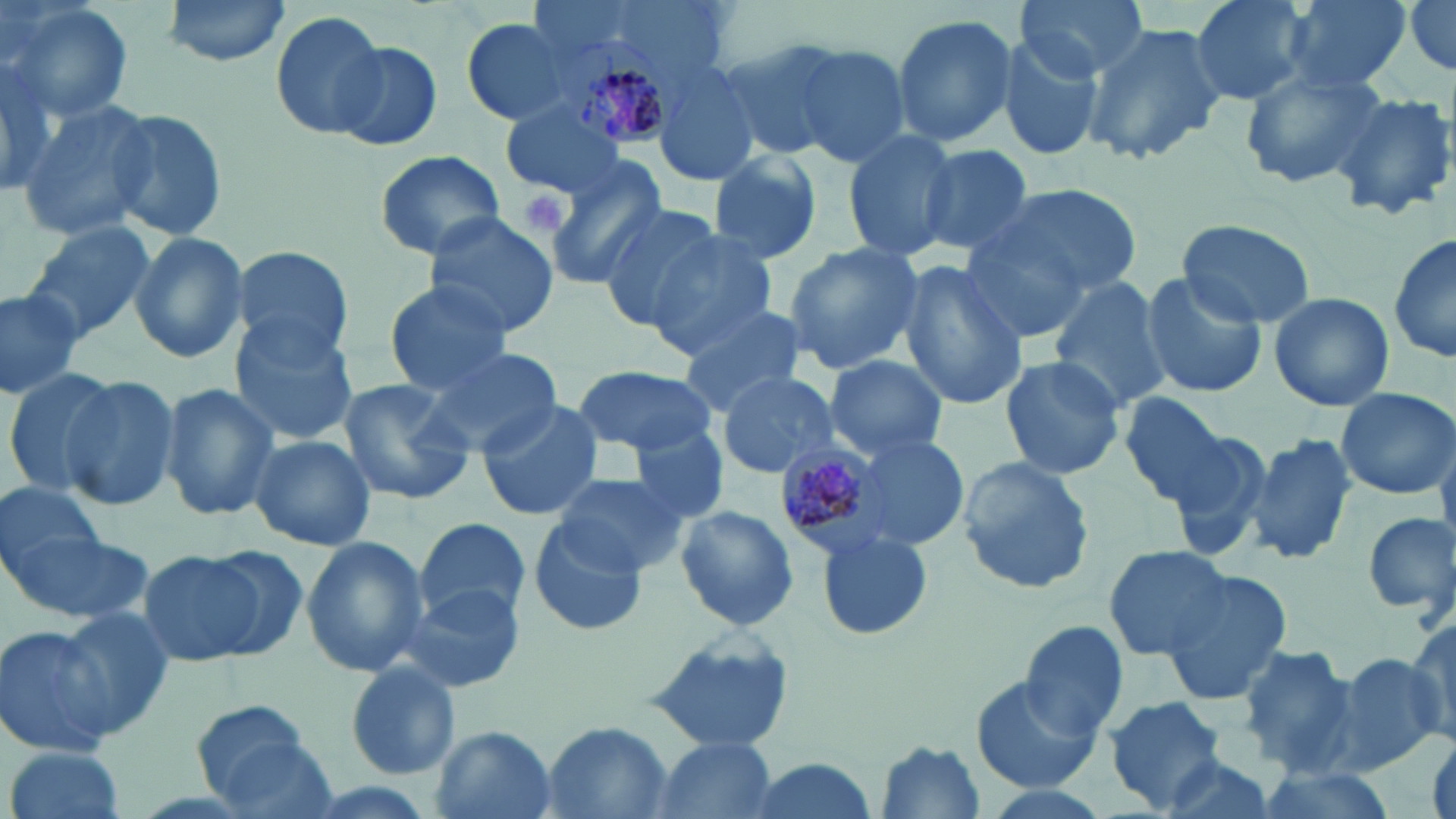

Approximate bounding boxes as [x1, y1, x2, y2] in pixels. Uninfected red blood cell locations: [3, 0, 135, 122], [159, 0, 295, 67], [1015, 0, 1145, 80], [1190, 0, 1312, 105], [1277, 0, 1415, 95], [1402, 0, 1456, 78], [270, 10, 391, 140], [461, 11, 593, 127], [891, 15, 1018, 146], [1083, 22, 1225, 168], [993, 29, 1104, 164], [717, 35, 851, 160], [327, 39, 442, 149], [788, 43, 913, 171], [0, 44, 62, 200], [653, 62, 762, 188], [1241, 62, 1388, 191], [1330, 92, 1454, 220], [18, 98, 156, 242], [499, 102, 628, 199], [107, 108, 230, 244], [841, 129, 958, 262], [915, 143, 1035, 258], [371, 149, 507, 259], [707, 150, 824, 266], [544, 158, 666, 287], [997, 181, 1145, 299], [597, 203, 726, 329], [421, 213, 560, 338], [956, 214, 1100, 340], [1175, 219, 1316, 328], [21, 220, 155, 340], [128, 233, 250, 363], [645, 234, 777, 356], [1390, 234, 1455, 365], [785, 243, 927, 371], [228, 246, 358, 366], [896, 259, 1029, 409], [1138, 273, 1266, 399], [1046, 278, 1171, 409], [383, 280, 515, 393], [0, 286, 87, 399], [1267, 290, 1395, 412], [675, 301, 808, 418], [229, 320, 361, 445], [419, 344, 564, 456], [823, 353, 948, 459], [996, 355, 1127, 481], [570, 366, 718, 457], [2, 368, 121, 498], [715, 371, 840, 479], [60, 377, 181, 510], [334, 379, 476, 505], [157, 382, 279, 521], [1336, 387, 1455, 498], [1115, 389, 1245, 513], [475, 398, 604, 521], [630, 431, 728, 526], [1244, 432, 1357, 570], [247, 434, 376, 551], [854, 435, 969, 548], [954, 457, 1095, 595], [551, 473, 687, 577], [0, 480, 114, 592], [674, 505, 800, 631], [1360, 511, 1455, 619], [532, 513, 649, 635], [414, 516, 532, 625], [7, 517, 154, 628], [814, 528, 933, 643], [301, 535, 430, 678], [1102, 544, 1236, 659], [136, 547, 283, 669], [1158, 568, 1298, 705], [400, 582, 526, 694], [52, 607, 179, 737], [1405, 618, 1456, 740], [1018, 621, 1129, 740], [0, 623, 126, 758], [644, 631, 800, 752], [1235, 647, 1356, 769], [1325, 652, 1449, 774], [345, 663, 461, 780], [970, 673, 1103, 795], [1103, 696, 1231, 812], [191, 700, 328, 813], [543, 723, 673, 818], [430, 727, 557, 819], [650, 735, 779, 819], [876, 740, 987, 816], [5, 744, 130, 819], [1147, 752, 1282, 819], [736, 758, 884, 819], [1247, 766, 1395, 819]. Plasmodium malariae-infected red blood cell locations: [555, 35, 681, 147], [775, 441, 894, 560]. Platelet locations: [516, 189, 572, 237]. Slide-level diagnosis: Plasmodium malariae. One field of a larger specimen. May-Grünwald-Giemsa-stained preparation. Optical microscopy. Image is 1456×819 pixels. Captured at 1000x magnification. Thin blood film.